Assess this cell for malaria.
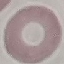

It is uninfected.

Photographed with a smartphone camera at the microscope eyepiece. Giemsa stain. Cell patch, automatically extracted from a larger field of view and resized to 64 × 64 pixels. Thin blood smear.